State which parasite is depicted.
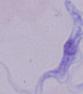

A trypanosome.

modality: photomicrograph
magnification: 1000x